Report the malaria status of this cell.
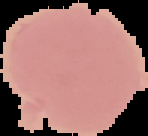

It is uninfected.

preparation = thin blood film
image type = cell region segmented out of the field of view; surrounding area masked to black
image size = 148×136 pixels